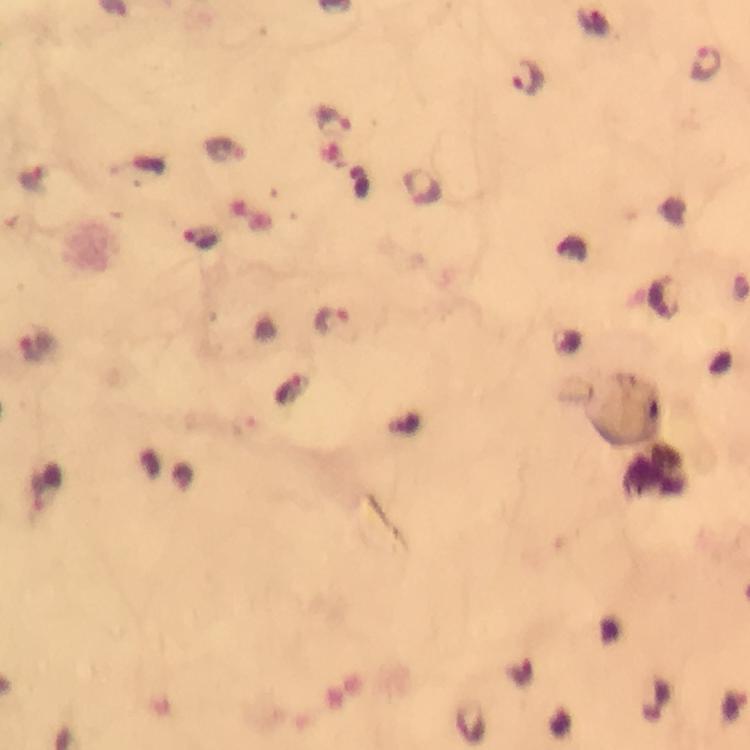

context = from a malaria diagnostic workup
capture = smartphone mounted on the microscope
malaria parasite locations = approximate object centers, in pixels from the top-left corner: (x=706, y=62), (x=528, y=77), (x=331, y=119), (x=422, y=184), (x=203, y=237), (x=331, y=320), (x=37, y=344), (x=44, y=486)
image size = 750×750 pixels
cropped from = a single field of view
immersion oil = used
stain = Giemsa
magnification = 100x
preparation = thick blood film